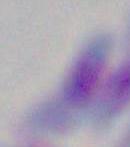
Summary:
  - Magnification: 1000x
  - Modality: micrograph
  - Identification: Toxoplasma gondii